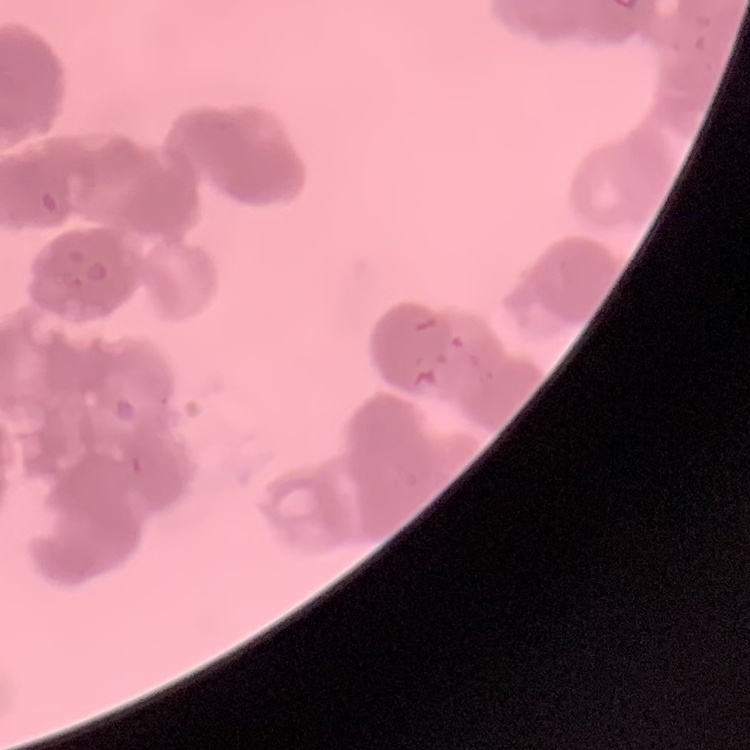
red blood cell morphology = rouleaux formation
preparation = thin blood film
image type = square crop of a larger photomicrograph
stain = Field's or Giemsa